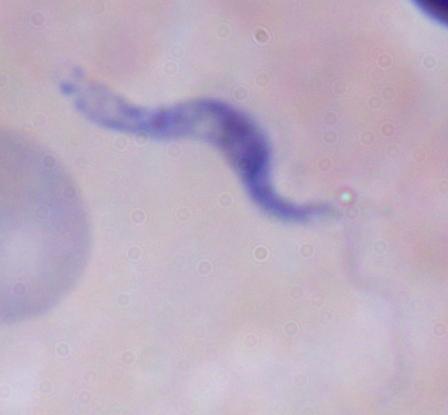 Captured at 1000x magnification. A trypanosome is seen. Micrograph.